Identify the cell.
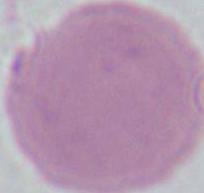

This is an erythrocyte.

magnification = 1000x
modality = photomicrograph